Assess this cell for malaria.
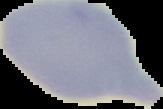
Uninfected.

preparation = thin blood smear
image size = 163×109 pixels
image type = cell region segmented out of the field of view; surrounding area masked to black